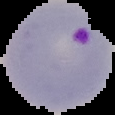
{
  "result": "malaria parasites detected",
  "preparation": "thin blood film",
  "image_type": "cell region segmented out of the field of view; surrounding area masked to black",
  "image_size": "115×115 pixels"
}